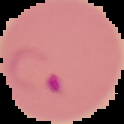
From a thin blood smear. Result: Plasmodium parasites detected. Cell region segmented out of the field of view; the surrounding area is masked to black. Image is 124×124 pixels.